Report the malaria status of this cell.
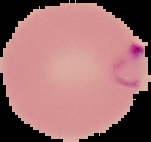
It is parasitized.

preparation = thin blood film
image type = cell region segmented out of the field of view; surrounding area masked to black
image size = 151×142 pixels